Name the blood parasite species.
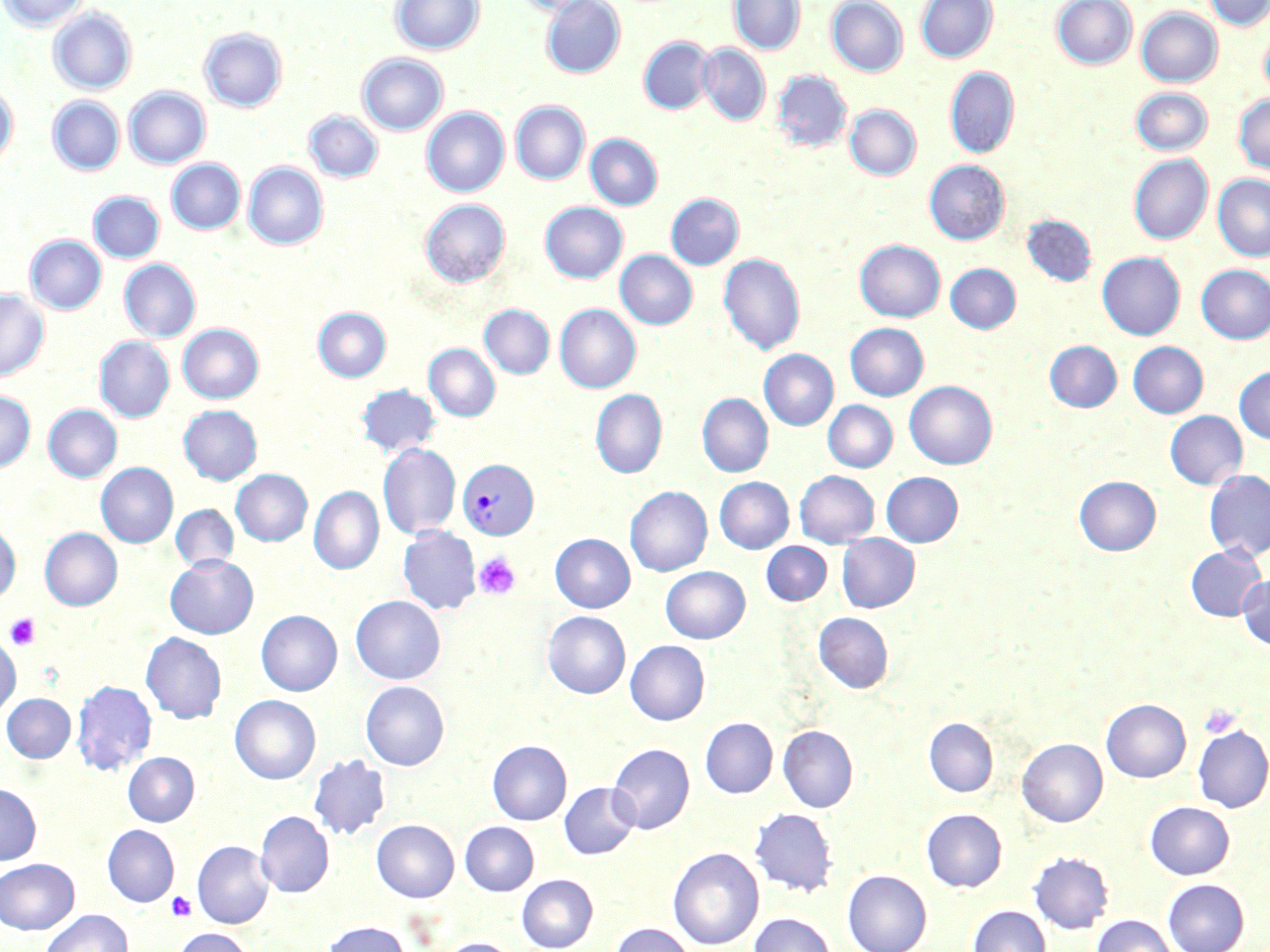
Plasmodium vivax.

platelet locations = approximate bounding boxes as named x1/y1/x2/y2 corners in pixels: (x1=474, y1=551, x2=521, y2=600), (x1=5, y1=613, x2=41, y2=650), (x1=1200, y1=704, x2=1242, y2=739), (x1=166, y1=891, x2=197, y2=921)
image size = 1270×952 pixels
magnification = 1000x
preparation = thin blood film
stain = May-Grünwald-Giemsa
modality = light microscopy
Plasmodium vivax-infected red blood cell locations = approximate bounding boxes as named x1/y1/x2/y2 corners in pixels: (x1=457, y1=460, x2=539, y2=540)
uninfected red blood cell locations = approximate bounding boxes as named x1/y1/x2/y2 corners in pixels: (x1=0, y1=0, x2=90, y2=31), (x1=391, y1=0, x2=484, y2=55), (x1=517, y1=0, x2=603, y2=16), (x1=729, y1=0, x2=805, y2=54), (x1=827, y1=0, x2=907, y2=76), (x1=916, y1=0, x2=997, y2=63), (x1=1051, y1=0, x2=1137, y2=69), (x1=1204, y1=0, x2=1269, y2=30), (x1=542, y1=1, x2=625, y2=78), (x1=49, y1=8, x2=137, y2=95), (x1=1137, y1=8, x2=1222, y2=86), (x1=1258, y1=25, x2=1270, y2=99), (x1=200, y1=28, x2=287, y2=112), (x1=639, y1=36, x2=715, y2=114), (x1=698, y1=44, x2=770, y2=125), (x1=357, y1=53, x2=448, y2=135), (x1=945, y1=66, x2=1019, y2=158), (x1=772, y1=71, x2=852, y2=152), (x1=0, y1=84, x2=18, y2=168), (x1=124, y1=86, x2=210, y2=169), (x1=1131, y1=87, x2=1213, y2=156), (x1=1233, y1=94, x2=1270, y2=176), (x1=47, y1=96, x2=124, y2=175), (x1=511, y1=101, x2=589, y2=184), (x1=845, y1=105, x2=921, y2=180), (x1=422, y1=107, x2=509, y2=196), (x1=304, y1=110, x2=383, y2=182), (x1=585, y1=134, x2=662, y2=210), (x1=1129, y1=155, x2=1213, y2=245), (x1=167, y1=159, x2=245, y2=234), (x1=924, y1=160, x2=1009, y2=245), (x1=243, y1=163, x2=328, y2=250), (x1=1213, y1=174, x2=1270, y2=261), (x1=89, y1=192, x2=164, y2=263), (x1=666, y1=193, x2=744, y2=269), (x1=420, y1=199, x2=510, y2=287), (x1=540, y1=202, x2=627, y2=283), (x1=1022, y1=214, x2=1097, y2=286), (x1=26, y1=235, x2=106, y2=314), (x1=855, y1=239, x2=945, y2=322), (x1=615, y1=250, x2=697, y2=329), (x1=719, y1=252, x2=805, y2=354), (x1=1097, y1=252, x2=1185, y2=340), (x1=119, y1=259, x2=200, y2=342), (x1=945, y1=263, x2=1021, y2=333), (x1=1196, y1=264, x2=1270, y2=344), (x1=0, y1=288, x2=48, y2=381), (x1=480, y1=304, x2=554, y2=379), (x1=555, y1=304, x2=641, y2=393), (x1=313, y1=307, x2=391, y2=382), (x1=845, y1=323, x2=928, y2=400), (x1=178, y1=324, x2=263, y2=404), (x1=94, y1=337, x2=174, y2=422), (x1=1044, y1=340, x2=1121, y2=412), (x1=1128, y1=342, x2=1208, y2=418), (x1=424, y1=344, x2=500, y2=422), (x1=759, y1=350, x2=838, y2=430), (x1=1234, y1=366, x2=1270, y2=444), (x1=905, y1=381, x2=997, y2=469), (x1=356, y1=384, x2=441, y2=457), (x1=591, y1=388, x2=667, y2=479), (x1=0, y1=390, x2=35, y2=472), (x1=697, y1=394, x2=773, y2=477), (x1=823, y1=400, x2=897, y2=472), (x1=44, y1=404, x2=121, y2=482), (x1=179, y1=405, x2=262, y2=484), (x1=1165, y1=411, x2=1247, y2=489), (x1=378, y1=443, x2=460, y2=540), (x1=96, y1=463, x2=178, y2=548), (x1=231, y1=469, x2=312, y2=546), (x1=795, y1=470, x2=879, y2=548), (x1=1204, y1=470, x2=1270, y2=562), (x1=881, y1=472, x2=963, y2=547), (x1=1074, y1=475, x2=1161, y2=555), (x1=715, y1=477, x2=794, y2=553), (x1=625, y1=486, x2=712, y2=576), (x1=309, y1=487, x2=383, y2=574), (x1=171, y1=505, x2=238, y2=572), (x1=0, y1=523, x2=20, y2=604), (x1=398, y1=526, x2=481, y2=615), (x1=41, y1=528, x2=122, y2=610), (x1=551, y1=534, x2=635, y2=612), (x1=837, y1=534, x2=919, y2=612), (x1=761, y1=542, x2=832, y2=606), (x1=1185, y1=546, x2=1268, y2=621), (x1=165, y1=555, x2=258, y2=639), (x1=661, y1=566, x2=749, y2=643), (x1=1237, y1=574, x2=1270, y2=650), (x1=351, y1=595, x2=445, y2=685), (x1=257, y1=610, x2=342, y2=696), (x1=543, y1=611, x2=630, y2=698), (x1=813, y1=612, x2=894, y2=693), (x1=141, y1=632, x2=227, y2=724), (x1=0, y1=634, x2=20, y2=717), (x1=625, y1=640, x2=709, y2=725), (x1=72, y1=680, x2=156, y2=775), (x1=361, y1=681, x2=449, y2=770), (x1=1, y1=693, x2=75, y2=762), (x1=230, y1=695, x2=320, y2=784), (x1=1101, y1=699, x2=1191, y2=782), (x1=700, y1=717, x2=777, y2=798), (x1=924, y1=717, x2=998, y2=797), (x1=1193, y1=724, x2=1270, y2=813), (x1=778, y1=725, x2=858, y2=812), (x1=1017, y1=738, x2=1107, y2=827), (x1=487, y1=740, x2=571, y2=825), (x1=608, y1=743, x2=694, y2=834), (x1=123, y1=752, x2=199, y2=826), (x1=308, y1=753, x2=390, y2=841), (x1=559, y1=782, x2=639, y2=859), (x1=0, y1=783, x2=41, y2=864), (x1=1145, y1=801, x2=1234, y2=879), (x1=749, y1=808, x2=838, y2=896), (x1=921, y1=808, x2=1006, y2=892), (x1=255, y1=811, x2=334, y2=897), (x1=372, y1=819, x2=459, y2=902), (x1=460, y1=821, x2=538, y2=896), (x1=103, y1=825, x2=179, y2=907), (x1=193, y1=840, x2=273, y2=928), (x1=668, y1=847, x2=764, y2=949), (x1=1028, y1=851, x2=1113, y2=934), (x1=0, y1=858, x2=79, y2=934), (x1=843, y1=869, x2=931, y2=952), (x1=517, y1=874, x2=598, y2=951), (x1=1163, y1=879, x2=1249, y2=952), (x1=967, y1=905, x2=1050, y2=952), (x1=41, y1=909, x2=133, y2=952), (x1=749, y1=912, x2=838, y2=952), (x1=1091, y1=914, x2=1177, y2=952), (x1=321, y1=921, x2=411, y2=952), (x1=609, y1=923, x2=696, y2=952), (x1=173, y1=928, x2=255, y2=952), (x1=437, y1=937, x2=518, y2=952)
field of view = one of a larger specimen